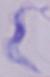
magnification = 1000x
modality = micrograph
identification = trypanosome